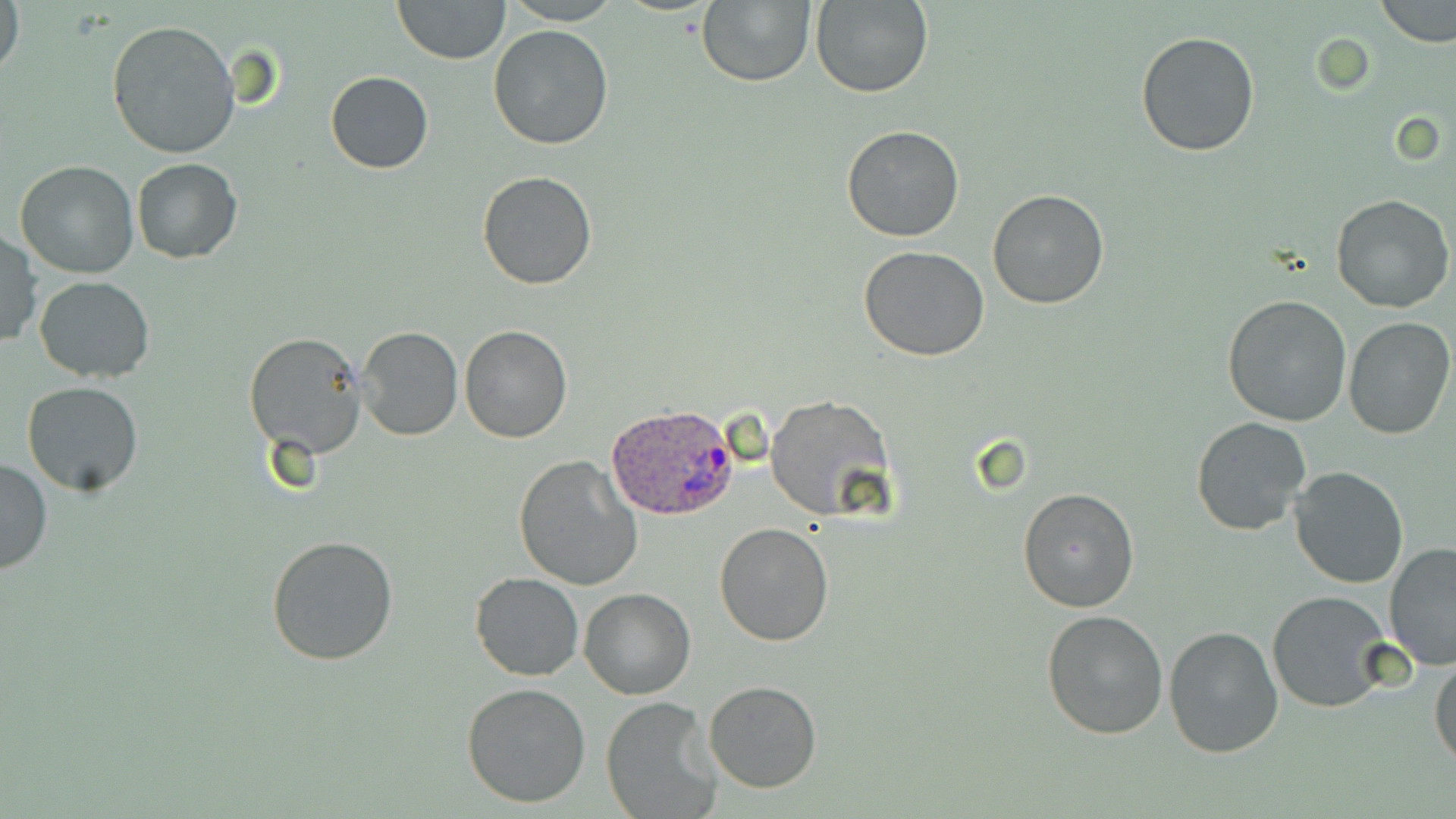

Approximate bounding boxes as named x1/y1/x2/y2 corners in pixels. Plasmodium ovale-infected red blood cell locations: (x1=605, y1=403, x2=739, y2=523). Uninfected red blood cell locations: (x1=1, y1=0, x2=24, y2=82), (x1=392, y1=0, x2=510, y2=64), (x1=504, y1=0, x2=619, y2=25), (x1=696, y1=0, x2=816, y2=87), (x1=809, y1=0, x2=933, y2=99), (x1=1375, y1=0, x2=1455, y2=48), (x1=107, y1=20, x2=240, y2=159), (x1=487, y1=24, x2=615, y2=150), (x1=1134, y1=30, x2=1260, y2=158), (x1=326, y1=71, x2=434, y2=174), (x1=841, y1=124, x2=965, y2=242), (x1=131, y1=158, x2=242, y2=262), (x1=14, y1=161, x2=140, y2=279), (x1=477, y1=171, x2=598, y2=291), (x1=988, y1=190, x2=1110, y2=309), (x1=1331, y1=193, x2=1453, y2=314), (x1=0, y1=230, x2=41, y2=350), (x1=859, y1=246, x2=990, y2=363), (x1=33, y1=275, x2=157, y2=383), (x1=1222, y1=294, x2=1352, y2=428), (x1=1343, y1=316, x2=1455, y2=440), (x1=458, y1=324, x2=572, y2=443), (x1=357, y1=326, x2=462, y2=441), (x1=243, y1=332, x2=368, y2=460), (x1=22, y1=381, x2=143, y2=495), (x1=764, y1=394, x2=894, y2=522), (x1=1191, y1=417, x2=1311, y2=537), (x1=512, y1=455, x2=643, y2=593), (x1=0, y1=456, x2=52, y2=576), (x1=1289, y1=464, x2=1409, y2=589), (x1=1017, y1=486, x2=1141, y2=614), (x1=715, y1=523, x2=833, y2=646), (x1=266, y1=533, x2=400, y2=668), (x1=1383, y1=541, x2=1456, y2=670), (x1=470, y1=573, x2=583, y2=680), (x1=579, y1=587, x2=695, y2=700), (x1=1268, y1=591, x2=1395, y2=713), (x1=1040, y1=608, x2=1168, y2=740), (x1=1164, y1=626, x2=1285, y2=758), (x1=1429, y1=654, x2=1456, y2=772), (x1=703, y1=680, x2=823, y2=793), (x1=461, y1=682, x2=592, y2=809), (x1=600, y1=697, x2=721, y2=819). Slide-level diagnosis: Plasmodium ovale. Optical microscopy. Thin blood smear. Single field of view. May-Grünwald-Giemsa stain. Image is 1456×819 pixels. 1000x magnification.